Identify the parasite.
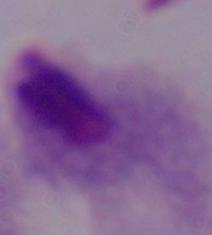

This is a trichomonad.

Summary:
  - Magnification: 1000x
  - Modality: photomicrograph